Point out each Plasmodium parasite.
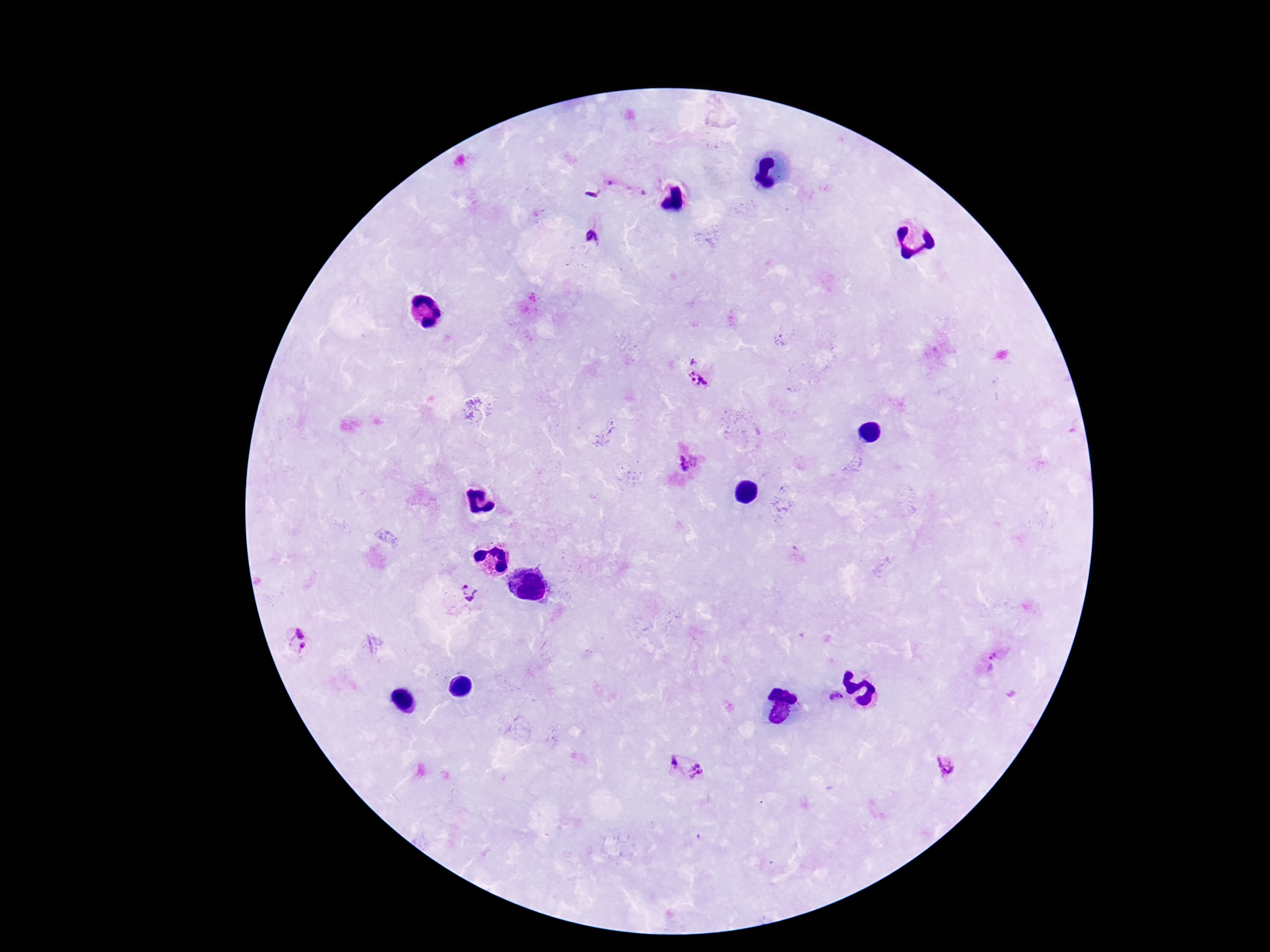

Approximate centers as (x, y) in pixels.
Plasmodium parasites: (592, 193), (592, 236), (692, 360), (698, 380), (687, 462), (468, 592), (299, 639), (998, 654), (836, 696), (673, 759), (944, 765), (698, 770).

Giemsa stain. Smartphone photograph taken through the microscope eyepiece. 100x magnification. One field from this slide. Image is 1270×952 pixels. Patient malaria status: positive. Thick peripheral-blood smear.